Outline platelets.
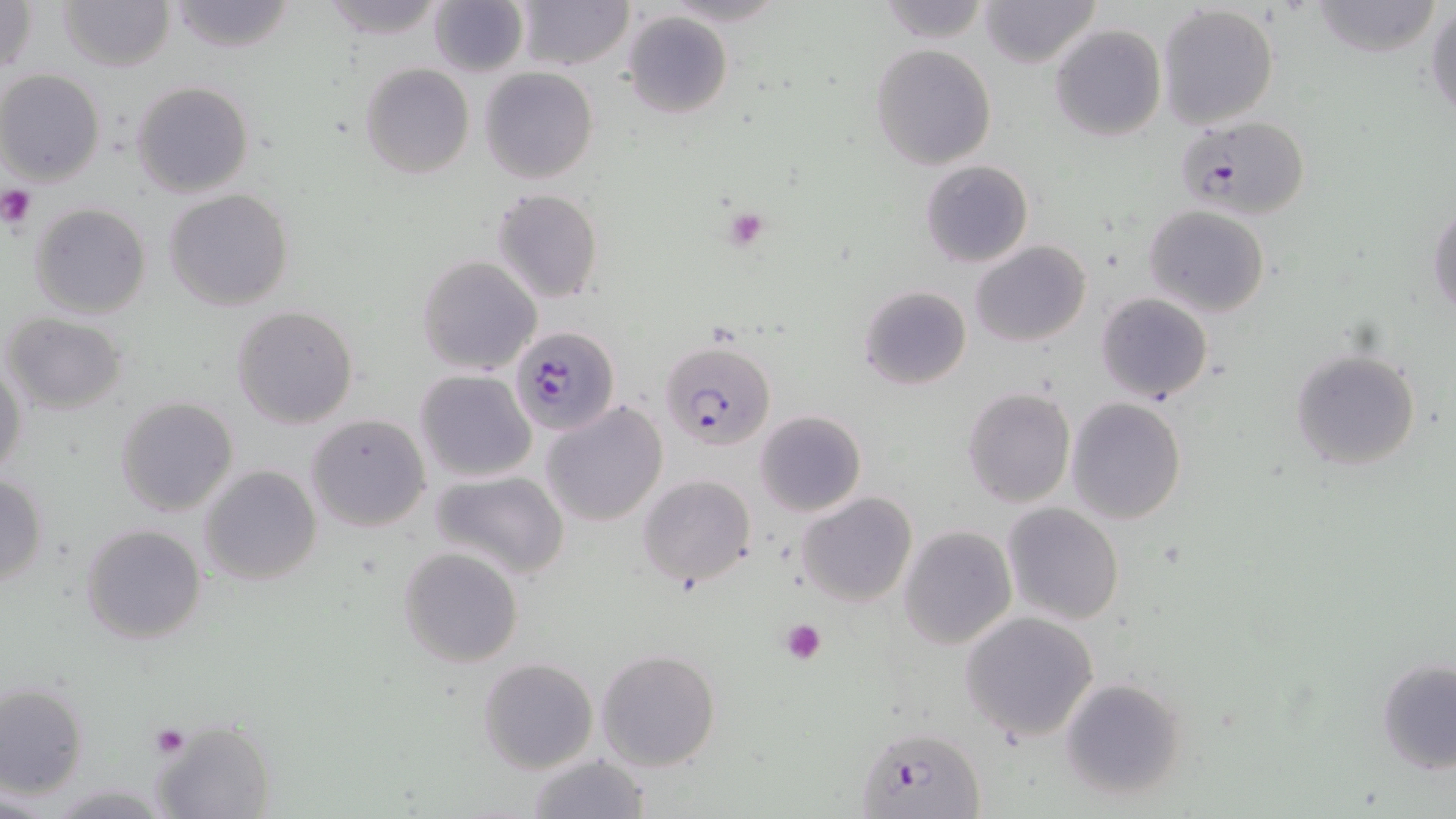
Approximate bounding boxes as [x1, y1, x2, y2] in pixels.
Platelets: [0, 186, 38, 228], [721, 204, 773, 252], [779, 617, 829, 663], [151, 725, 189, 758].

Uninfected red blood cell locations: [59, 0, 174, 72], [166, 0, 297, 54], [318, 0, 446, 41], [513, 0, 632, 71], [979, 0, 1101, 68], [1, 1, 39, 79], [428, 1, 527, 78], [1310, 1, 1442, 56], [870, 2, 992, 42], [1157, 4, 1280, 129], [1426, 4, 1456, 123], [624, 12, 732, 119], [1050, 24, 1165, 140], [871, 43, 996, 171], [359, 62, 475, 179], [480, 67, 598, 184], [0, 70, 105, 186], [130, 80, 255, 199], [919, 160, 1032, 269], [163, 189, 295, 312], [491, 189, 603, 304], [439, 199, 574, 346], [29, 202, 153, 318], [1428, 203, 1456, 316], [1144, 205, 1270, 316], [970, 240, 1091, 347], [417, 255, 541, 374], [859, 285, 972, 390], [1095, 292, 1213, 403], [232, 306, 359, 430], [3, 313, 129, 416], [1289, 347, 1424, 470], [0, 357, 29, 481], [414, 369, 537, 484], [961, 387, 1075, 508], [115, 397, 238, 517], [1065, 397, 1187, 524], [542, 401, 669, 526], [754, 409, 867, 516], [306, 412, 432, 533], [198, 464, 323, 586], [430, 469, 570, 581], [0, 473, 49, 588], [638, 474, 757, 591], [796, 492, 918, 608], [1002, 502, 1124, 625], [79, 524, 205, 645], [898, 526, 1017, 649], [397, 547, 524, 667], [960, 610, 1099, 744], [595, 648, 722, 773], [478, 657, 598, 773], [1376, 658, 1456, 774], [1058, 676, 1190, 805], [1, 680, 90, 800], [150, 720, 274, 819], [527, 753, 651, 819]. Plasmodium falciparum-infected red blood cell locations: [1176, 115, 1309, 220], [511, 326, 620, 435], [658, 340, 775, 451], [859, 726, 985, 818]. Slide-level diagnosis: Plasmodium falciparum. 1000x magnification. May-Grünwald-Giemsa-stained preparation. Thin blood film. Optical microscopy. Image is 1456×819 pixels. One field of a larger specimen.